Point out each malaria parasite.
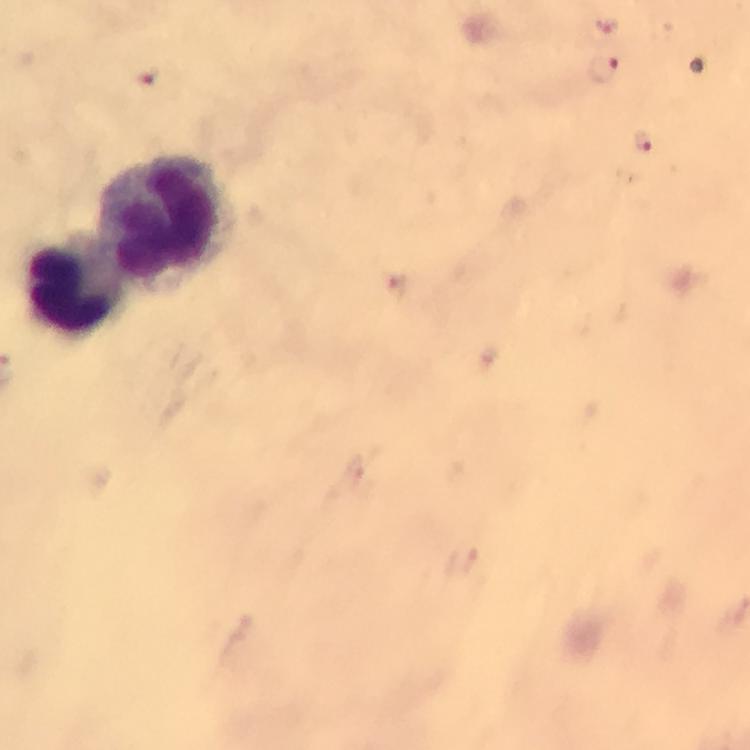
Approximate centers as {x, y} in pixels.
Malaria parasites: {600, 69}, {149, 75}, {644, 141}.

Leukocyte locations: {167, 218}, {79, 282}. Image is 750×750 pixels. Photographed with a smartphone mounted on the microscope. Cropped region of a single field of view. Thick smear. Immersion oil was used. 100x magnification. Giemsa-stained preparation. From a malaria diagnostic workup.